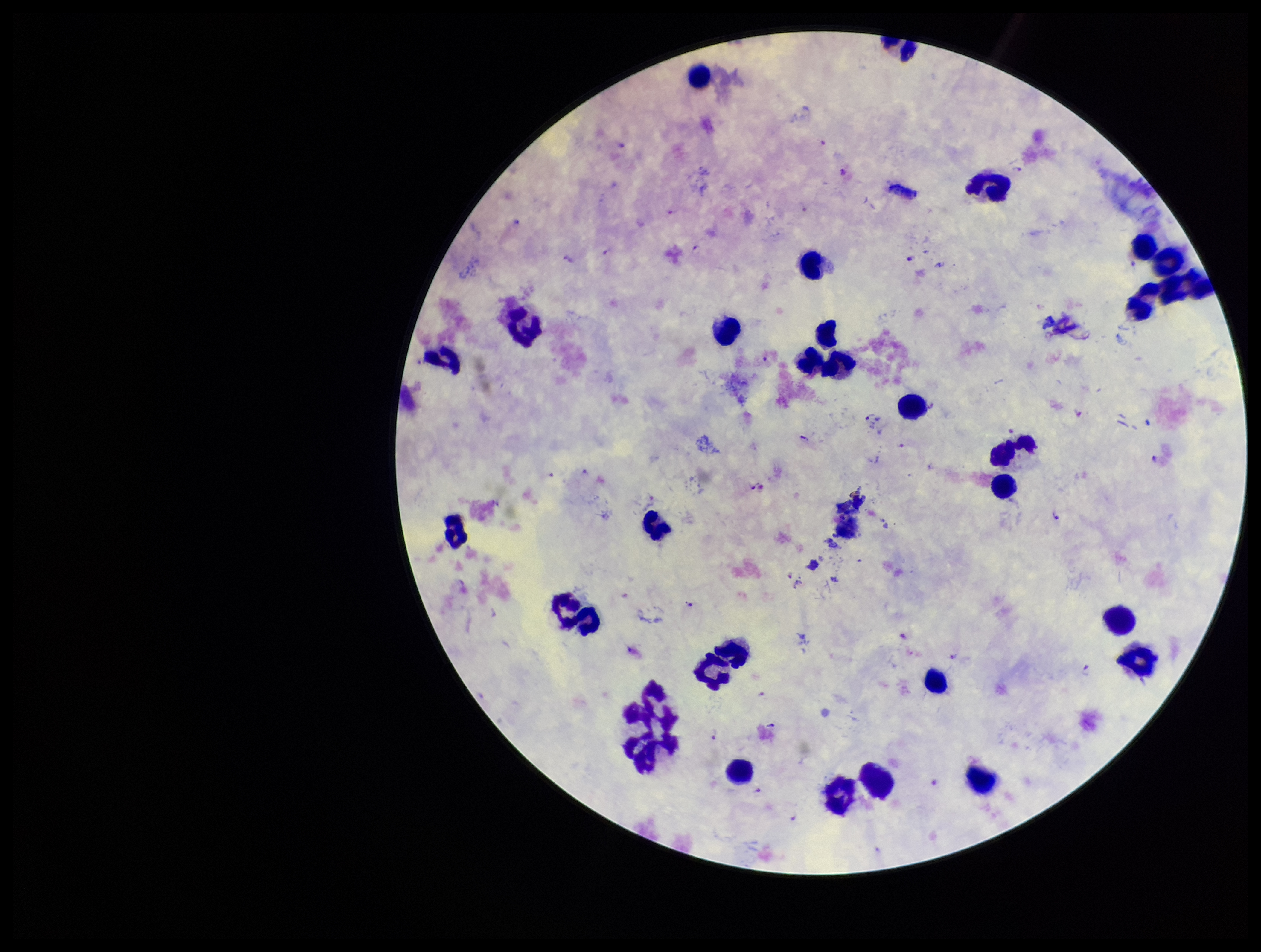
Summary:
  - Species reported for this patient: Plasmodium falciparum
  - Capture: smartphone photograph through the microscope eyepiece
  - Field of view: single
  - Leukocyte count: 27
  - Preparation: thick smear
  - Image size: 1261×952 pixels
  - Patient malaria status: positive
  - Parasite count: 13
  - Plasmodium parasites: identified
  - Stain: Giemsa